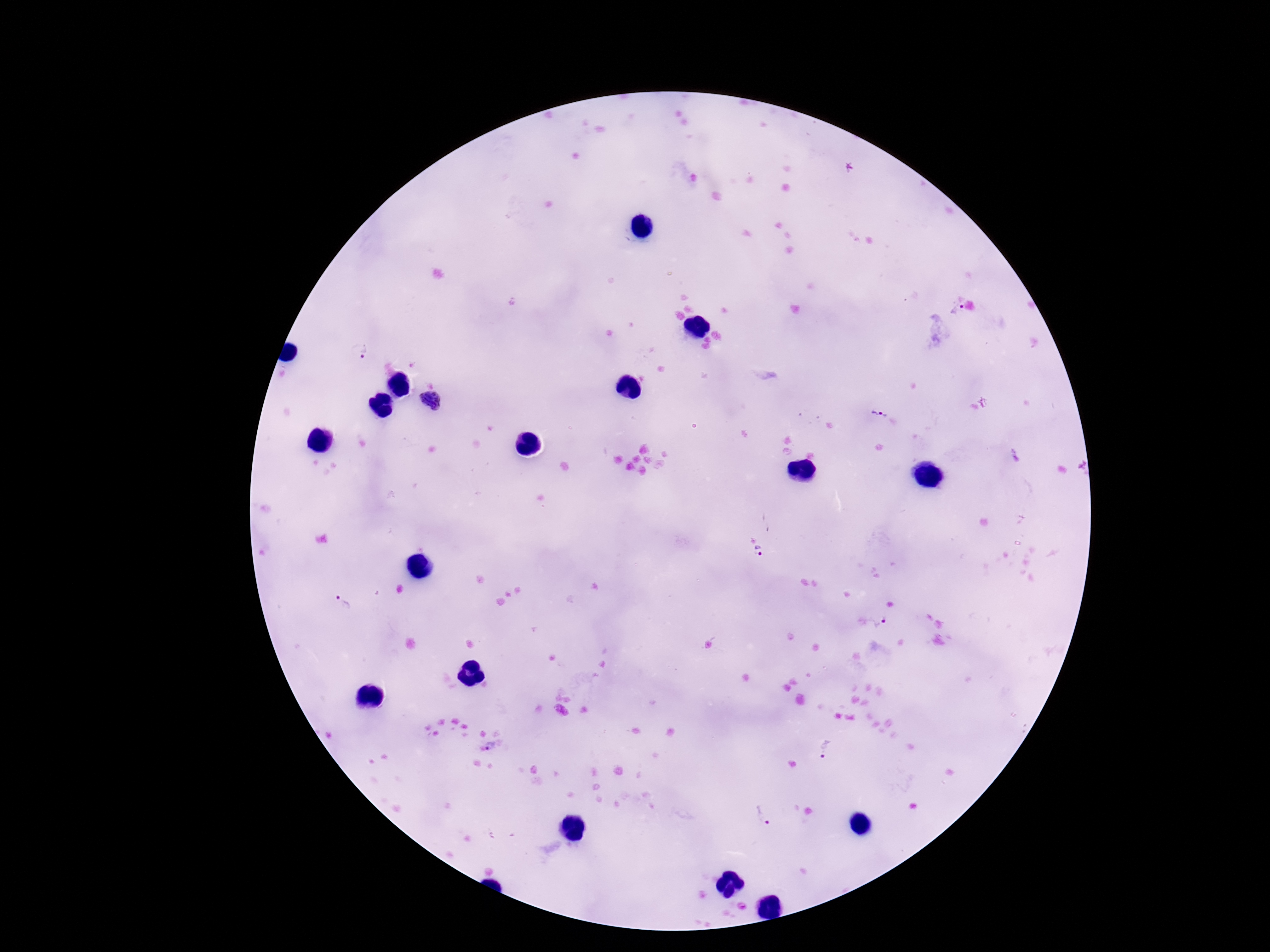
Approximate centers as (x, y) in pixels.
Summary:
  - Plasmodium parasite locations: (955, 307), (364, 351), (984, 401), (431, 403), (877, 414), (760, 553), (339, 601), (881, 623), (495, 746), (824, 750), (762, 817)
  - Field of view: one from this slide
  - Capture: smartphone camera through the microscope eyepiece
  - Magnification: 100x
  - Preparation: thick peripheral-blood smear
  - Patient malaria status: infected
  - Image size: 1270×952 pixels
  - Stain: Giemsa